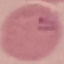

Summary:
  - Malaria status: uninfected
  - Stain: Giemsa
  - Capture: smartphone camera at the microscope eyepiece
  - Preparation: thin smear
  - Image type: automatically extracted cell patch, resized to 64 × 64 pixels